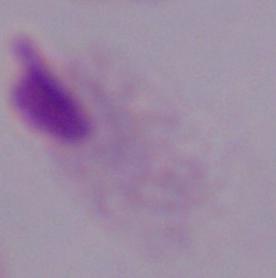
Summary:
  - Magnification: 1000x
  - Identification: trichomonad
  - Modality: photomicrograph